Classify this cell by malaria status.
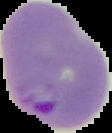

It is parasitized.

Summary:
  - Preparation: thin blood smear
  - Image type: segmented cell region with the area outside set to black
  - Image size: 112×133 pixels